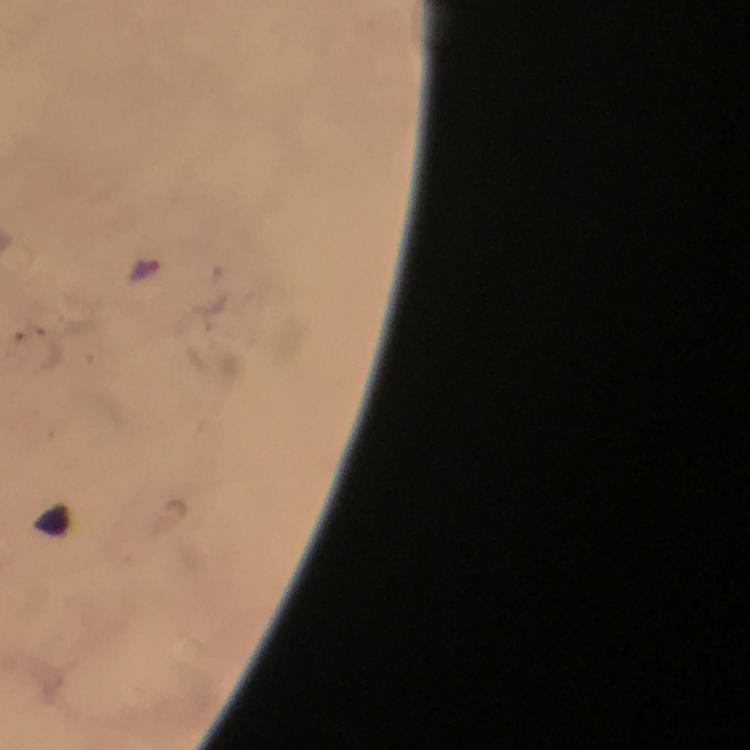

{
  "image_size": "750×750 pixels",
  "stain": "Giemsa",
  "capture": "smartphone camera through the microscope",
  "immersion_oil": "used",
  "cropped_from": "a single field of view",
  "preparation": "thick smear",
  "context": "from a diagnostic examination for malaria",
  "magnification": "100x",
  "malaria_parasite_locations": "approximate centers as (x, y) in pixels: (147, 268)"
}